Report the malaria status of this cell.
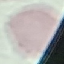
It is uninfected.

Summary:
  - Stain: Giemsa
  - Preparation: thin smear
  - Capture: smartphone camera at the microscope eyepiece
  - Image type: automatically extracted cell patch, resized to 64 × 64 pixels